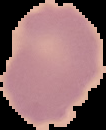
Summary:
  - Image type: segmented cell region on a black background
  - Image size: 106×130 pixels
  - Malaria status: uninfected
  - Preparation: thin blood film